Give the location of every parasitized red blood cell.
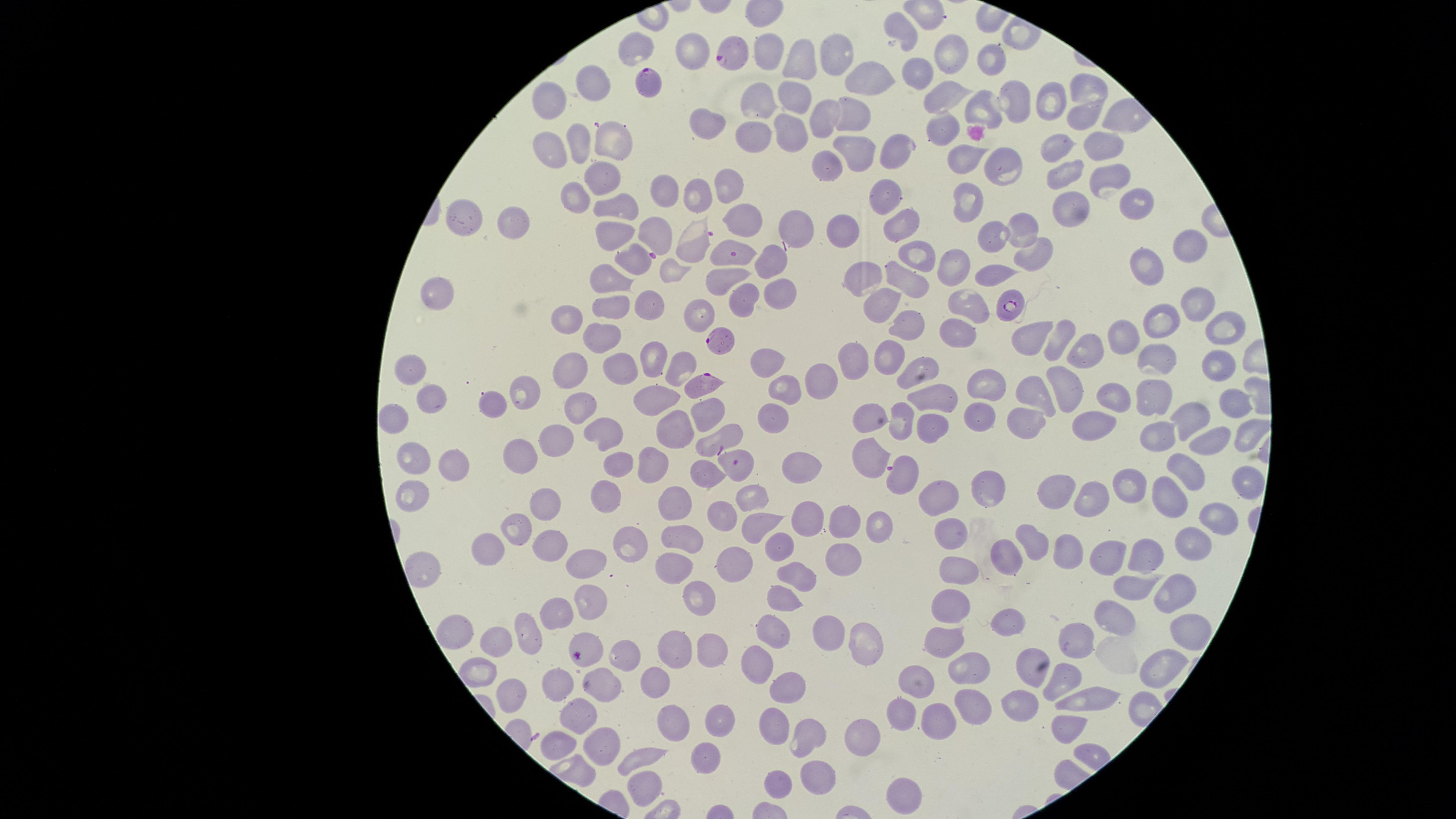
Approximate marker points as (x, y) in pixels.
Parasitized red blood cells: (730, 50), (645, 80), (897, 150), (734, 253), (1012, 299), (717, 339), (703, 383), (722, 435), (739, 462), (901, 473), (586, 651).

field of view = single
stain = Giemsa
visible region = circular
capture = smartphone photograph through the microscope eyepiece
uninfected red blood cells = approximate marker points as (x, y) in pixels: (904, 32), (638, 46), (694, 51), (762, 51), (954, 54), (839, 55), (987, 59), (805, 60), (917, 72), (592, 75), (866, 81), (1085, 87), (945, 89), (796, 95), (548, 96), (756, 100), (1050, 100), (975, 106), (1013, 106), (851, 111), (1084, 116), (819, 118), (945, 126), (707, 129), (793, 130), (612, 139), (752, 139), (1093, 140), (576, 141), (551, 148), (854, 148), (1053, 148), (827, 159), (965, 161), (1008, 168), (593, 169), (1112, 170), (1061, 177), (732, 186), (661, 188), (697, 190), (891, 195), (1134, 202), (619, 203), (972, 204), (1067, 209), (463, 215), (746, 218), (513, 222), (901, 223), (798, 225), (1019, 226), (840, 230), (620, 231), (654, 233), (992, 236), (689, 243), (1189, 244), (1036, 250), (922, 251), (633, 256), (769, 262), (953, 263), (1150, 267), (723, 274), (988, 277), (607, 279), (912, 281), (866, 282), (779, 288), (441, 291), (648, 302), (748, 302), (882, 302), (964, 305), (1197, 305), (609, 306), (698, 311), (565, 318), (908, 327), (1166, 327), (1224, 330), (601, 333), (962, 335), (1038, 339), (1121, 339), (1061, 342), (1086, 353), (650, 354), (886, 354), (764, 358), (1163, 360), (853, 361), (618, 363), (678, 363), (1218, 364), (914, 365), (413, 369), (571, 370), (1064, 375), (822, 384), (986, 385), (1034, 385), (534, 391), (784, 391), (659, 392), (1157, 396), (938, 397), (1117, 397), (434, 398), (1232, 402), (492, 404), (580, 407), (710, 408), (771, 413), (866, 413), (1192, 417), (973, 418), (395, 421), (1029, 421), (1089, 421), (901, 422), (603, 428), (674, 428), (935, 432), (1242, 433), (1159, 435), (1210, 440), (557, 442), (525, 451), (874, 458), (618, 460), (649, 460), (412, 463), (800, 465), (1180, 465), (452, 470), (705, 470), (1241, 475), (1129, 482), (1168, 491), (1052, 492), (989, 493), (752, 494), (603, 497), (943, 498), (1084, 500), (412, 501), (544, 503), (677, 505), (1214, 513), (722, 515), (809, 519), (759, 522), (841, 522), (878, 525), (519, 527), (950, 532), (684, 533), (631, 542), (1190, 542), (545, 544), (1027, 545), (492, 548), (779, 549), (1063, 549), (1148, 553), (849, 556), (1116, 556), (729, 559), (1003, 561), (426, 568), (670, 568), (581, 571), (957, 574), (802, 576), (1139, 585), (1167, 590), (701, 594), (785, 596), (588, 602), (951, 605), (556, 611), (1118, 619), (1004, 623), (826, 626), (773, 628), (453, 629), (1181, 631), (1079, 634), (530, 635), (498, 641), (951, 641), (862, 643), (670, 650), (709, 650), (622, 659), (1027, 663), (761, 664), (1158, 668), (483, 670), (967, 672), (1064, 681), (557, 682), (920, 682), (603, 683), (653, 685), (789, 688), (505, 691), (1090, 700), (1022, 707), (970, 709), (901, 710), (578, 718), (716, 718), (934, 722), (675, 724), (775, 726), (1064, 729), (805, 737), (604, 739), (863, 745), (553, 748), (646, 755), (705, 757), (818, 777), (780, 779), (644, 785), (900, 796)
preparation = thin blood smear
image size = 1456×819 pixels
species = Plasmodium falciparum